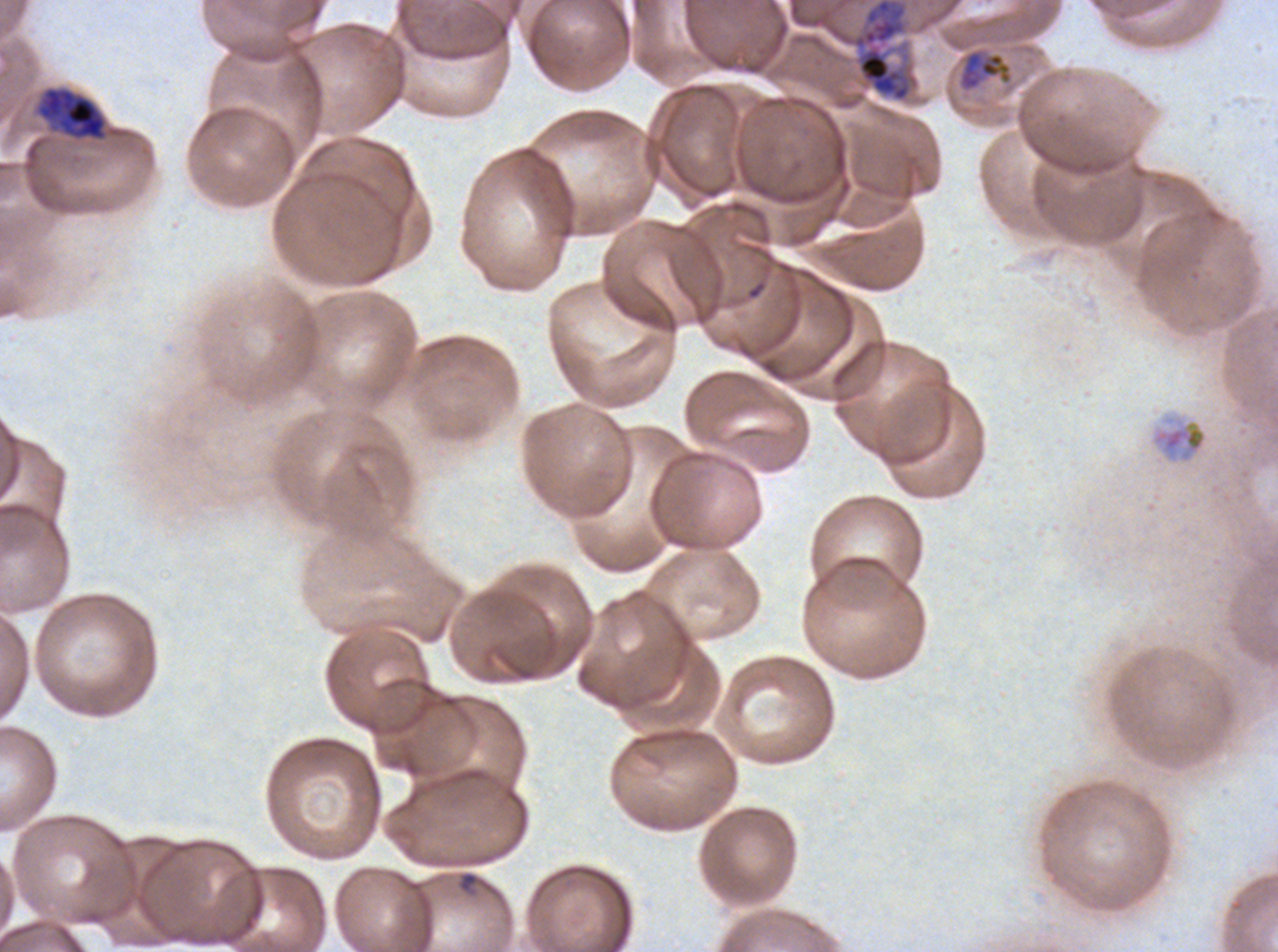
Approximate bounding boxes as [x1, y1, x2, y2] in pixels.
Summary:
  - Ring locations: [458, 871, 479, 893]
  - Late trophozoite locations: [36, 86, 106, 140], [1149, 412, 1210, 466]
  - Mid trophozoite locations: [959, 50, 1012, 91]
  - Early schizont locations: [851, 0, 912, 103]
  - Field of view: sub-image separated from a larger composite
  - Life-cycle stages observed: ring, mid trophozoite, late trophozoite, early schizont
  - Image size: 1278×952 pixels
  - Specimen: P. falciparum from a patient in The Gambia, cultured ex vivo for 24 to 48 hours
  - Preparation: thin blood film
  - Stain: Giemsa